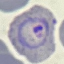

Result: malaria parasites detected. Giemsa stain. Acquired by smartphone through the microscope eyepiece. Thin smear of blood. Automatically extracted cell patch, resized to 64 × 64 pixels.